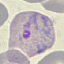
{
  "result": "malaria parasites detected",
  "capture": "smartphone through the microscope eyepiece",
  "stain": "Giemsa",
  "image_type": "automatically extracted cell patch, resized to 64 × 64 pixels",
  "preparation": "thin smear"
}